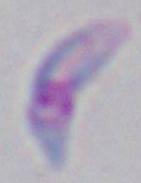

magnification = 1000x
modality = photomicrograph
identification = Toxoplasma gondii